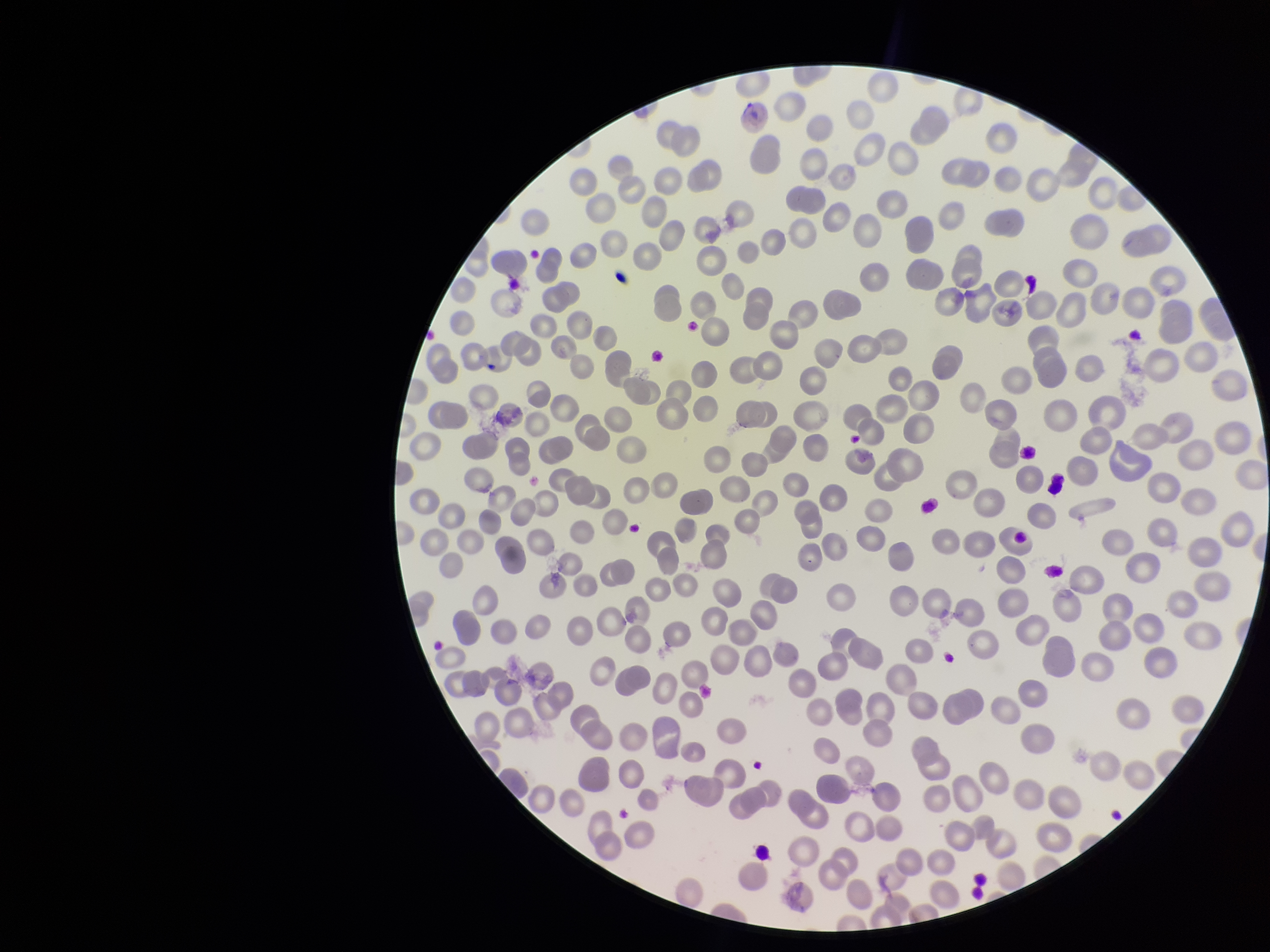
Summary:
  - Stain: Giemsa
  - Capture: smartphone photograph through the microscope eyepiece
  - Parasitized red blood cells: none seen
  - Red blood cell count: 296
  - Field of view: one from this slide
  - Species reported for this patient: Plasmodium falciparum
  - Image size: 1270×952 pixels
  - Preparation: thin
  - Parasitized red blood cell count: 0
  - Patient malaria status: positive